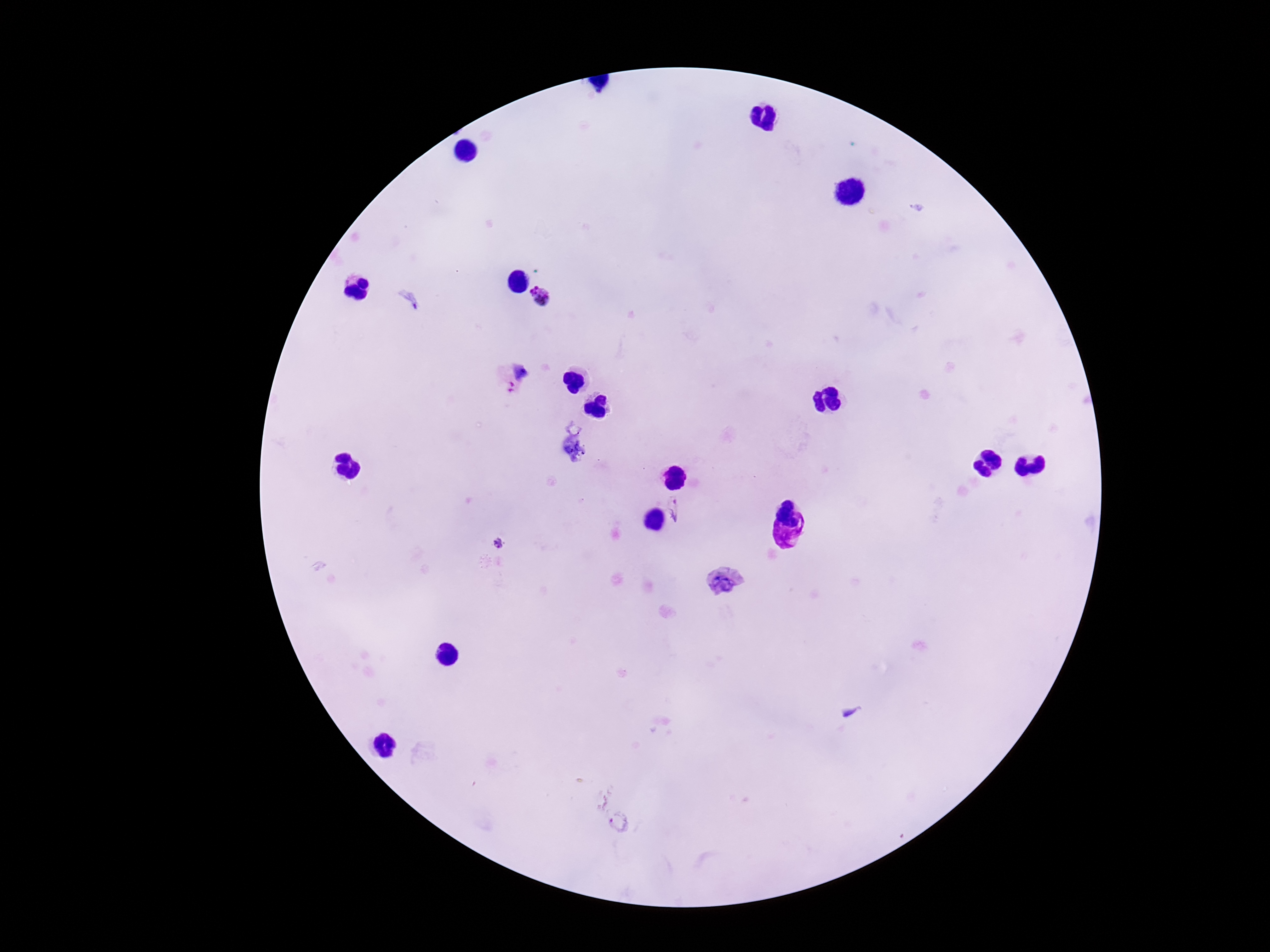
Approximate centers as (x, y) in pixels.
Summary:
  - Plasmodium parasite locations: (541, 297), (520, 369), (677, 508), (499, 543), (619, 823)
  - Patient malaria status: positive
  - Image size: 1270×952 pixels
  - Preparation: thick blood film
  - Capture: smartphone camera through the microscope eyepiece
  - Stain: Giemsa
  - Field of view: single
  - Magnification: 100x